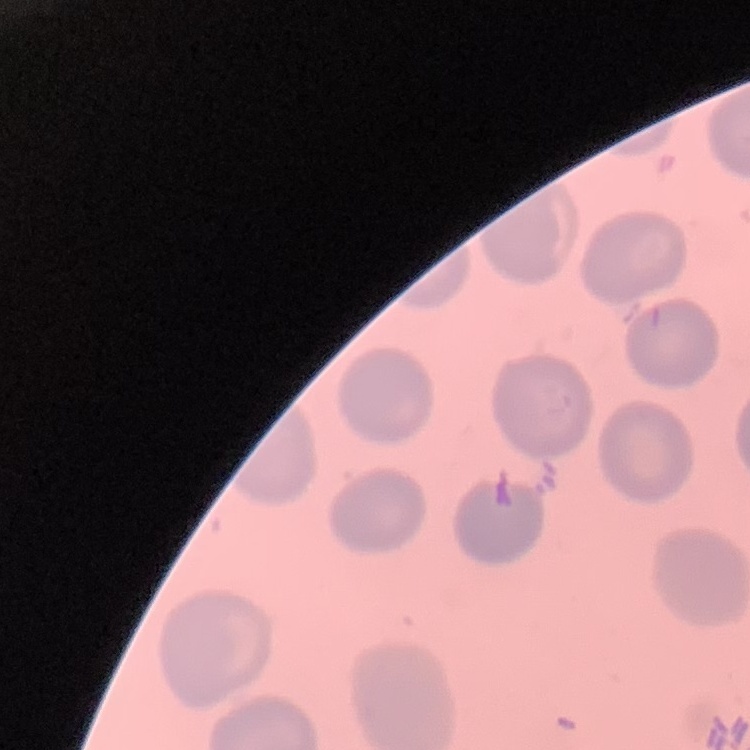
red blood cell morphology = no rouleaux formation
image type = one tile cut from a larger photomicrograph
stain = Field's or Giemsa
preparation = thin blood film